Report the malaria status of this cell.
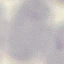

Uninfected.

Thin blood smear. Photographed with a smartphone camera at the microscope eyepiece. Cell patch, automatically extracted from a larger field of view and resized to 64 × 64 pixels. Giemsa stain.